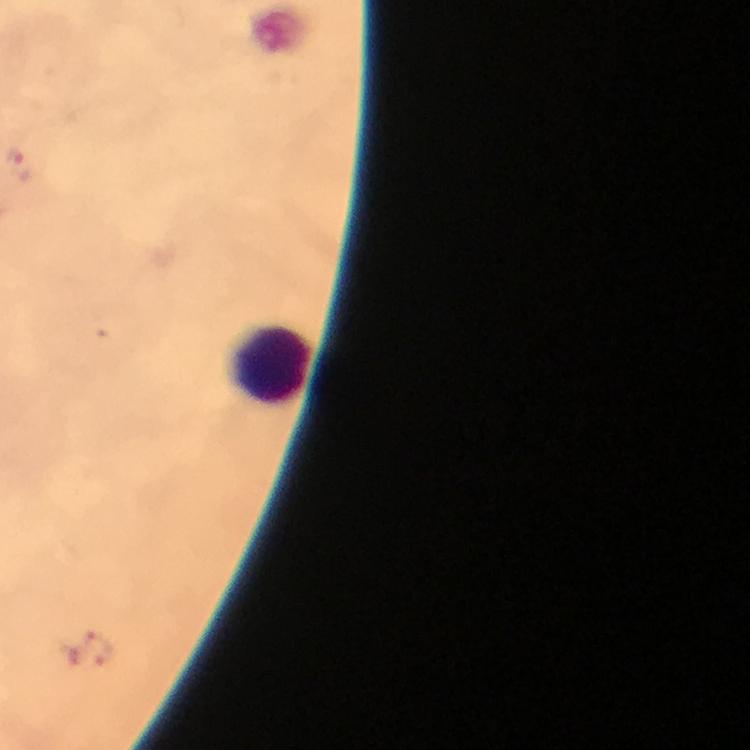 Approximate centers as [x, y] in pixels. Leukocyte locations: [268, 362]. Malaria parasite locations: [89, 650]. A crop from one field of view. Smartphone photograph taken through a microscope. Thick blood smear. Giemsa-stained preparation. 100x magnification. Immersion oil was used. From a malaria diagnostic workup. Image is 750×750 pixels.